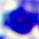
{
  "identification": "leukocyte",
  "magnification": "400x",
  "modality": "photomicrograph"
}